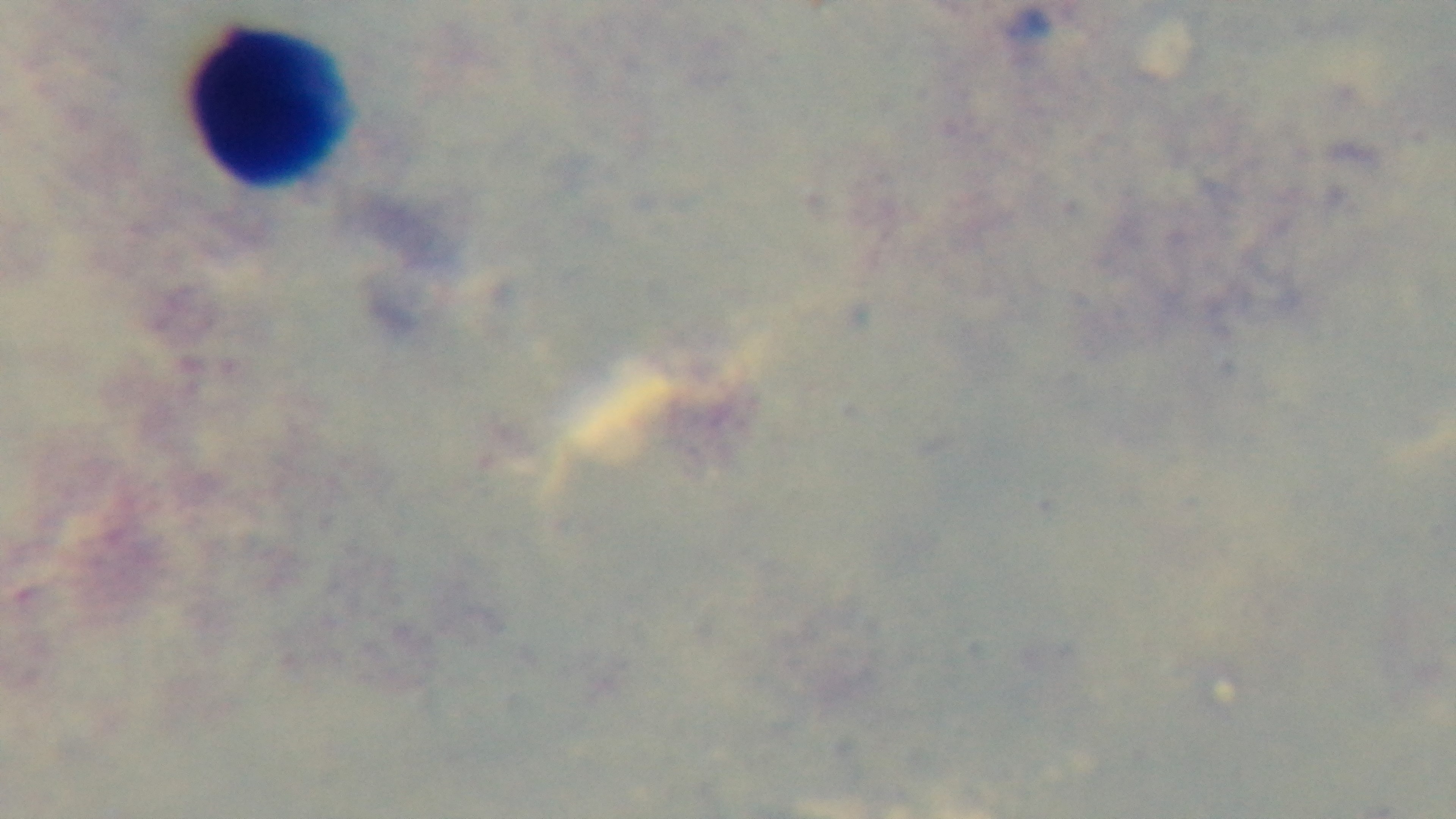
{
  "preparation": "thick blood film",
  "objective": "100x oil immersion",
  "stain": "Giemsa",
  "malaria_status": "uninfected",
  "modality": "light microscopy",
  "capture": "mounted 4K digital camera",
  "field_of_view": "single"
}